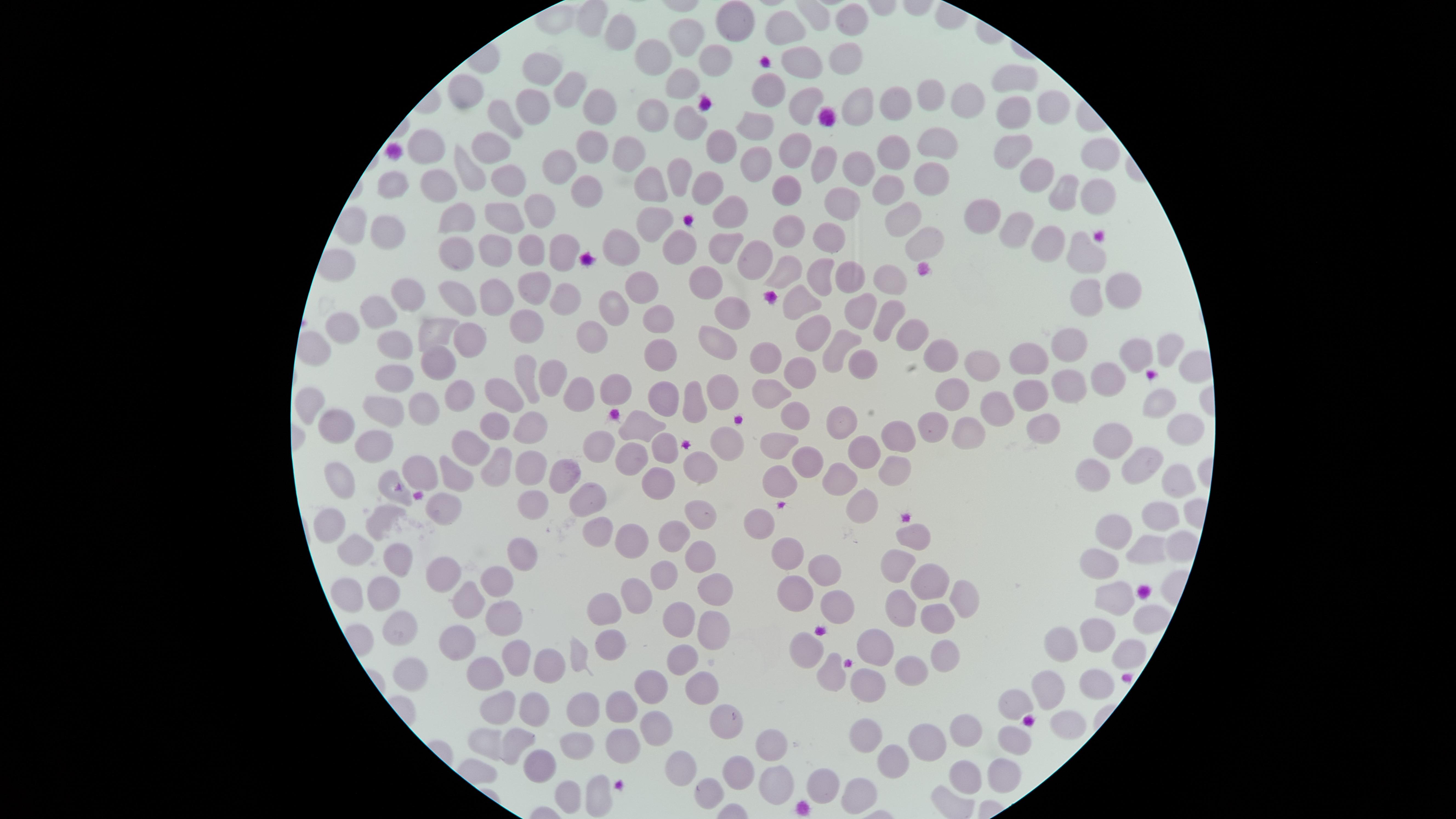

Approximate marker points as {x, y} in pixels.
Summary:
  - Uninfected RBCs: {585, 19}, {726, 20}, {853, 21}, {788, 28}, {612, 34}, {685, 34}, {844, 57}, {650, 58}, {707, 62}, {792, 63}, {1011, 76}, {536, 77}, {682, 77}, {769, 84}, {565, 90}, {460, 92}, {926, 97}, {961, 98}, {800, 100}, {1045, 101}, {599, 107}, {855, 107}, {890, 107}, {649, 109}, {1009, 109}, {531, 112}, {500, 119}, {684, 121}, {748, 123}, {928, 140}, {491, 142}, {423, 147}, {584, 147}, {1009, 147}, {789, 150}, {714, 151}, {1092, 153}, {890, 154}, {617, 158}, {822, 162}, {755, 163}, {854, 169}, {555, 170}, {1034, 173}, {472, 175}, {928, 178}, {675, 180}, {395, 185}, {438, 185}, {507, 185}, {657, 188}, {582, 191}, {892, 191}, {1053, 192}, {706, 196}, {784, 198}, {838, 201}, {1093, 201}, {726, 205}, {544, 209}, {455, 215}, {500, 215}, {980, 215}, {646, 217}, {904, 223}, {1010, 228}, {385, 230}, {789, 230}, {923, 238}, {829, 240}, {625, 243}, {677, 244}, {557, 245}, {1044, 246}, {526, 248}, {459, 251}, {494, 251}, {718, 256}, {750, 261}, {1080, 262}, {791, 273}, {814, 273}, {848, 275}, {892, 277}, {698, 280}, {537, 282}, {630, 285}, {409, 289}, {497, 289}, {1122, 289}, {455, 296}, {1081, 296}, {566, 298}, {795, 298}, {727, 303}, {372, 310}, {614, 312}, {857, 312}, {886, 315}, {661, 317}, {909, 332}, {430, 333}, {535, 333}, {590, 333}, {342, 336}, {810, 336}, {466, 341}, {395, 342}, {711, 346}, {1066, 348}, {1160, 348}, {836, 351}, {651, 353}, {765, 356}, {1132, 356}, {937, 359}, {862, 360}, {436, 361}, {1020, 361}, {553, 368}, {972, 369}, {523, 372}, {1104, 372}, {797, 374}, {398, 383}, {1057, 383}, {617, 387}, {575, 389}, {470, 390}, {724, 391}, {506, 395}, {949, 395}, {772, 396}, {1026, 396}, {1160, 400}, {665, 402}, {697, 402}, {309, 404}, {422, 408}, {383, 409}, {992, 412}, {796, 417}, {337, 418}, {839, 419}, {929, 420}, {519, 424}, {641, 424}, {492, 426}, {1042, 427}, {895, 429}, {967, 430}, {1182, 432}, {1116, 436}, {365, 441}, {723, 441}, {661, 443}, {782, 443}, {601, 447}, {471, 448}, {865, 448}, {632, 454}, {1137, 454}, {809, 455}, {693, 465}, {497, 466}, {424, 468}, {528, 469}, {890, 472}, {337, 473}, {458, 473}, {832, 476}, {1080, 476}, {565, 478}, {776, 480}, {651, 481}, {1180, 481}, {396, 495}, {534, 499}, {590, 500}, {858, 505}, {443, 507}, {705, 513}, {761, 516}, {1161, 516}, {382, 520}, {326, 524}, {594, 528}, {1118, 528}, {914, 530}, {665, 533}, {630, 539}, {1151, 546}, {518, 552}, {785, 552}, {356, 553}, {694, 553}, {396, 561}, {1097, 562}, {899, 565}, {663, 572}, {813, 574}, {493, 576}, {638, 589}, {926, 589}, {381, 592}, {1113, 593}, {964, 594}, {345, 596}, {460, 596}, {793, 596}, {715, 598}, {842, 601}, {895, 604}, {1141, 616}, {602, 618}, {935, 618}, {504, 620}, {677, 623}, {397, 626}, {1095, 631}, {708, 638}, {1068, 638}, {453, 641}, {608, 646}, {804, 646}, {874, 649}, {580, 651}, {940, 653}, {1123, 653}, {516, 655}, {680, 656}, {908, 665}, {549, 667}, {481, 671}, {410, 673}, {829, 675}, {1101, 678}, {868, 681}, {644, 684}, {698, 684}, {1051, 688}, {619, 703}, {1008, 707}, {583, 708}, {535, 709}, {493, 714}, {725, 722}, {1060, 724}, {651, 726}, {969, 728}, {867, 732}, {770, 736}, {515, 738}, {1017, 738}, {618, 741}, {483, 744}, {921, 746}, {578, 749}, {886, 761}, {540, 762}, {680, 766}, {742, 769}, {995, 772}, {964, 774}, {772, 779}, {821, 786}, {708, 788}, {856, 788}, {568, 789}, {597, 794}
  - Preparation: thin blood film
  - Image size: 1456×819 pixels
  - Stain: Giemsa
  - Capture: smartphone photograph through the microscope eyepiece
  - Field of view: single
  - Presence: no malaria parasites identified
  - Visible region: circular